Locate every Plasmodium ovale-infected red blood cell.
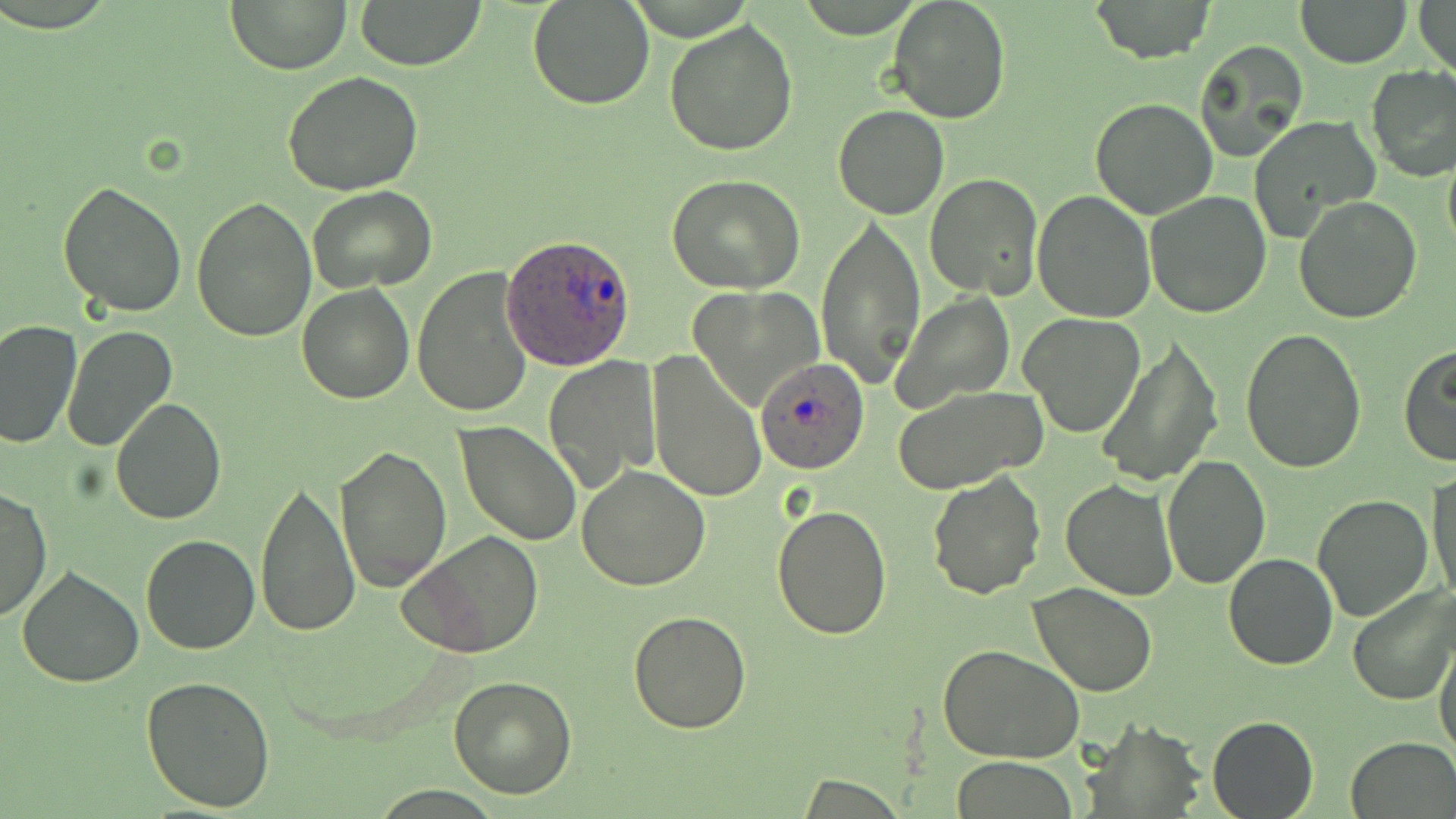
Approximate bounding boxes as (x1,y1)-(x2,y2) corner pairs in pixels.
Plasmodium ovale-infected red blood cells: (502,236)-(637,368), (755,358)-(870,474).

Uninfected red blood cell locations: (225,0)-(352,73), (354,0)-(488,69), (887,0)-(1011,124), (1087,0)-(1215,63), (1296,0)-(1411,69), (1415,0)-(1455,76), (528,1)-(655,111), (664,19)-(799,157), (1195,40)-(1311,160), (1366,66)-(1456,181), (282,70)-(424,195), (1090,98)-(1218,220), (832,104)-(950,220), (1248,114)-(1381,240), (1442,151)-(1456,257), (926,173)-(1043,301), (666,174)-(810,295), (59,182)-(188,319), (308,186)-(438,292), (1032,190)-(1158,322), (1145,191)-(1272,318), (190,195)-(316,342), (1294,195)-(1422,323), (816,215)-(926,385), (412,267)-(536,419), (297,284)-(413,404), (689,285)-(823,410), (893,290)-(1015,412), (1017,312)-(1147,437), (0,320)-(82,449), (62,323)-(178,452), (1239,327)-(1368,474), (1097,338)-(1222,487), (1398,345)-(1456,467), (646,352)-(766,502), (542,356)-(661,493), (892,384)-(1048,491), (111,397)-(227,523), (456,421)-(583,547), (334,444)-(451,592), (1161,456)-(1271,590), (365,463)-(490,626), (576,465)-(713,590), (1428,467)-(1455,607), (927,469)-(1047,600), (257,477)-(359,640), (1060,479)-(1180,601), (0,484)-(52,624), (1312,495)-(1433,621), (772,500)-(892,639), (399,531)-(545,658), (140,534)-(263,655), (1223,554)-(1336,670), (17,564)-(145,687), (1028,583)-(1159,697), (1348,585)-(1456,706), (626,609)-(752,733), (1434,636)-(1456,761), (936,644)-(1085,766), (141,674)-(277,813), (448,675)-(577,798), (1082,715)-(1207,815), (1207,715)-(1318,819), (1347,735)-(1456,817), (950,757)-(1081,817), (794,775)-(910,816). Slide-level diagnosis: Plasmodium ovale. One field of a larger specimen. Light microscopy. Thin blood smear. Captured at 1000x magnification. May-Grünwald-Giemsa-stained preparation. Image is 1456×819 pixels.